Comment on the morphology of the erythrocytes.
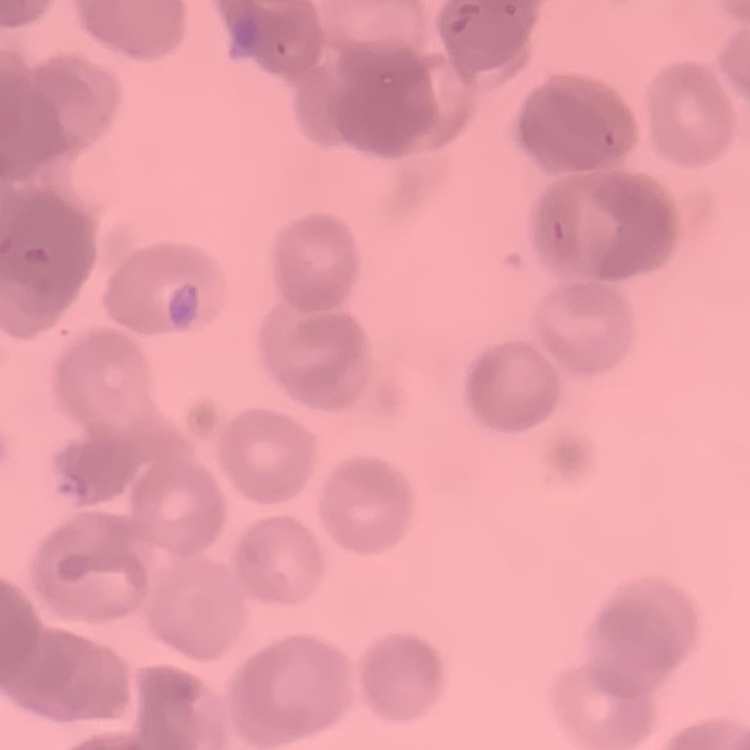
Rouleaux formation.

Summary:
  - Image type: square crop of a larger photomicrograph
  - Preparation: thin blood smear
  - Stain: Field's or Giemsa